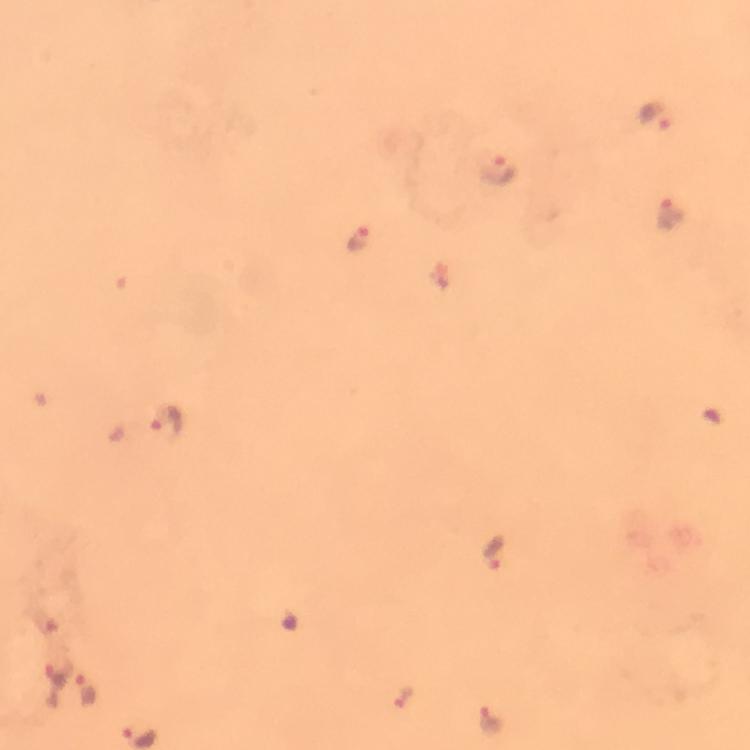

Approximate object centers, in pixels from the top-left corner.
Summary:
  - Plasmodium parasite locations: (x=657, y=117), (x=498, y=170), (x=671, y=215), (x=359, y=237), (x=167, y=422), (x=493, y=554), (x=55, y=682), (x=86, y=690), (x=405, y=698), (x=491, y=720)
  - Context: from a malaria diagnostic workup
  - Immersion oil: used
  - Capture: smartphone camera through the microscope
  - Magnification: 100x
  - Image size: 750×750 pixels
  - Cropped from: a single field of view
  - Stain: Giemsa
  - Preparation: thick smear